Draw a bounding box around every trophozoite.
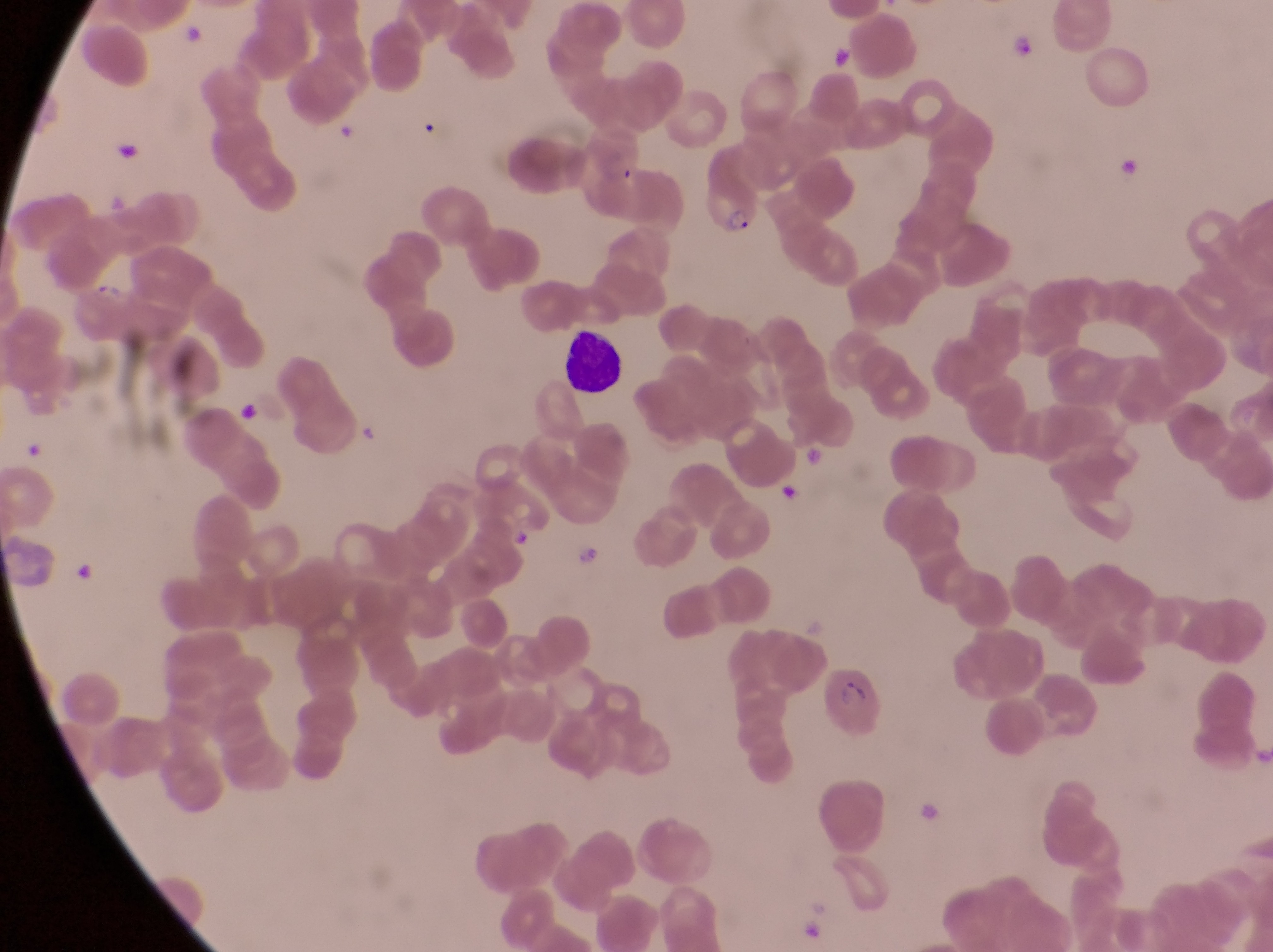
Approximate bounding boxes as {left, top, right, bottom} in pixels.
Trophozoites: {90, 278, 127, 305}, {232, 394, 262, 422}, {571, 544, 606, 577}.

Parasitised red blood cell locations: {697, 169, 764, 243}, {822, 664, 884, 746}. Leukocyte locations: {554, 325, 623, 397}. Thin blood smear. At a magnification of 1000x. Captured by a smartphone held over the eyepiece of an Olympus CX-23 microscope. Sample from Uganda. Image is 1273×952 pixels. One field of view.